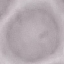

result: no malaria parasites seen
capture: smartphone through the microscope eyepiece
preparation: thin blood film
image_type: cell patch, automatically extracted from a larger field of view and resized to 64 × 64 pixels
stain: Giemsa